Point out every malaria parasite.
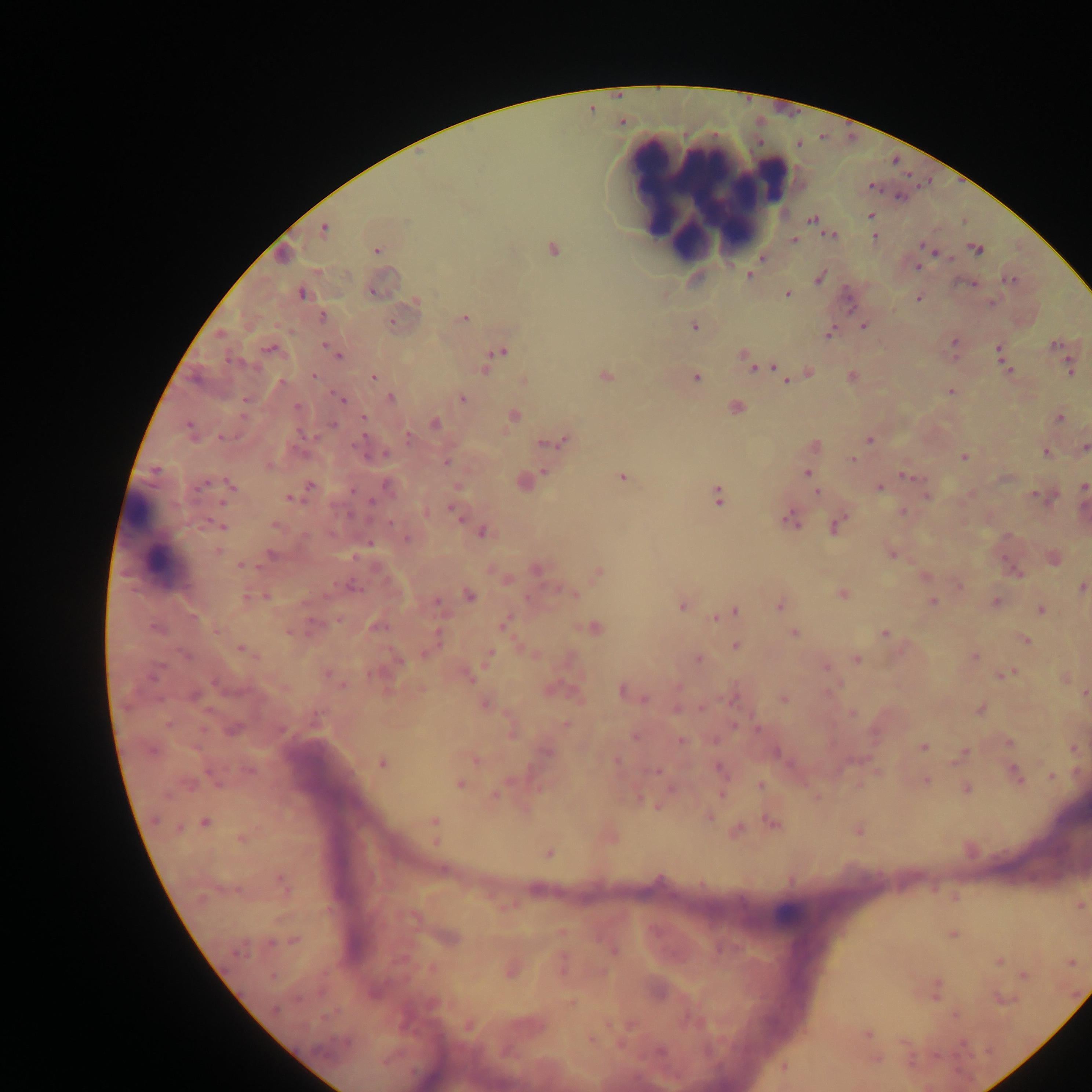

Approximate centers as (x, y) in pixels.
Malaria parasites: (870, 186), (870, 215), (812, 219), (323, 229), (824, 230), (832, 235), (874, 237), (793, 239), (922, 244), (975, 248), (552, 249), (376, 250), (933, 252), (282, 255), (763, 256), (918, 267), (748, 275), (819, 277), (1009, 279), (972, 284), (301, 293), (788, 293), (918, 297), (415, 302), (991, 302), (322, 317), (463, 318), (392, 322), (863, 325), (693, 326), (829, 332), (1055, 344), (327, 345), (954, 345), (269, 348), (497, 351), (999, 352), (742, 353), (337, 355), (1069, 366), (752, 367), (773, 367), (486, 369), (1008, 370), (808, 371), (314, 376), (605, 376), (851, 376), (372, 377), (695, 377), (524, 380), (786, 380), (950, 391), (390, 398), (462, 398), (342, 399), (734, 406), (514, 415), (1059, 418), (363, 419), (434, 423), (190, 430), (409, 437), (868, 439), (564, 440), (545, 442), (813, 446), (1084, 447), (1046, 451), (380, 454), (964, 456), (852, 459), (446, 460), (544, 470), (806, 473), (811, 475), (623, 476), (908, 477), (522, 482), (229, 486), (309, 486), (388, 486), (457, 486), (1083, 486), (878, 487), (816, 491), (969, 494), (718, 495), (926, 495), (1033, 495), (1043, 495), (289, 497), (454, 510), (902, 511), (791, 518), (837, 524), (221, 525), (276, 525), (482, 531), (406, 537), (369, 542), (217, 551), (890, 552), (1052, 558), (242, 565), (537, 569), (597, 572), (496, 573), (1017, 573), (503, 576), (925, 576), (958, 584), (351, 587), (1081, 587), (842, 592), (573, 593), (470, 595), (265, 596), (995, 601), (437, 602), (933, 602), (681, 603), (780, 604), (1041, 609), (732, 611), (720, 615), (503, 622), (375, 625), (594, 627), (794, 632), (884, 632), (436, 639), (1025, 639), (521, 645), (735, 645), (240, 648), (488, 657), (974, 657), (856, 658), (697, 659), (397, 660), (825, 666), (1006, 673), (328, 674), (466, 675), (1063, 677), (552, 688), (422, 689), (624, 691), (1084, 693), (783, 698), (485, 703), (677, 707), (979, 709), (852, 713), (733, 724), (566, 725), (232, 728), (758, 729), (635, 736), (679, 740), (1009, 742), (922, 747), (1074, 747), (546, 752), (776, 752), (963, 753), (473, 759), (616, 761), (381, 762), (720, 769), (655, 771), (1016, 774), (1051, 776), (925, 780), (459, 783), (759, 785), (859, 785), (671, 788), (965, 788), (721, 793), (494, 795), (817, 797), (656, 807), (708, 815), (433, 821), (772, 822), (204, 823), (857, 829), (735, 830), (435, 835), (608, 836), (242, 838), (548, 853), (443, 871), (282, 883), (954, 896), (1079, 905), (562, 932), (952, 934), (448, 938), (293, 941), (613, 950), (998, 960), (1071, 961), (562, 964), (511, 969), (1023, 975), (936, 990), (1000, 998), (571, 1001), (955, 1014), (468, 1024), (866, 1034), (590, 1039), (875, 1058), (783, 1067).

{
  "country": "Ghana",
  "leukocyte_locations": "approximate centers as (x, y) in pixels: (717, 202), (156, 539), (788, 915)",
  "preparation": "thick blood film",
  "field_of_view": "single",
  "capture": "mobile-phone photograph through a microscope",
  "image_size": "1092×1092 pixels"
}